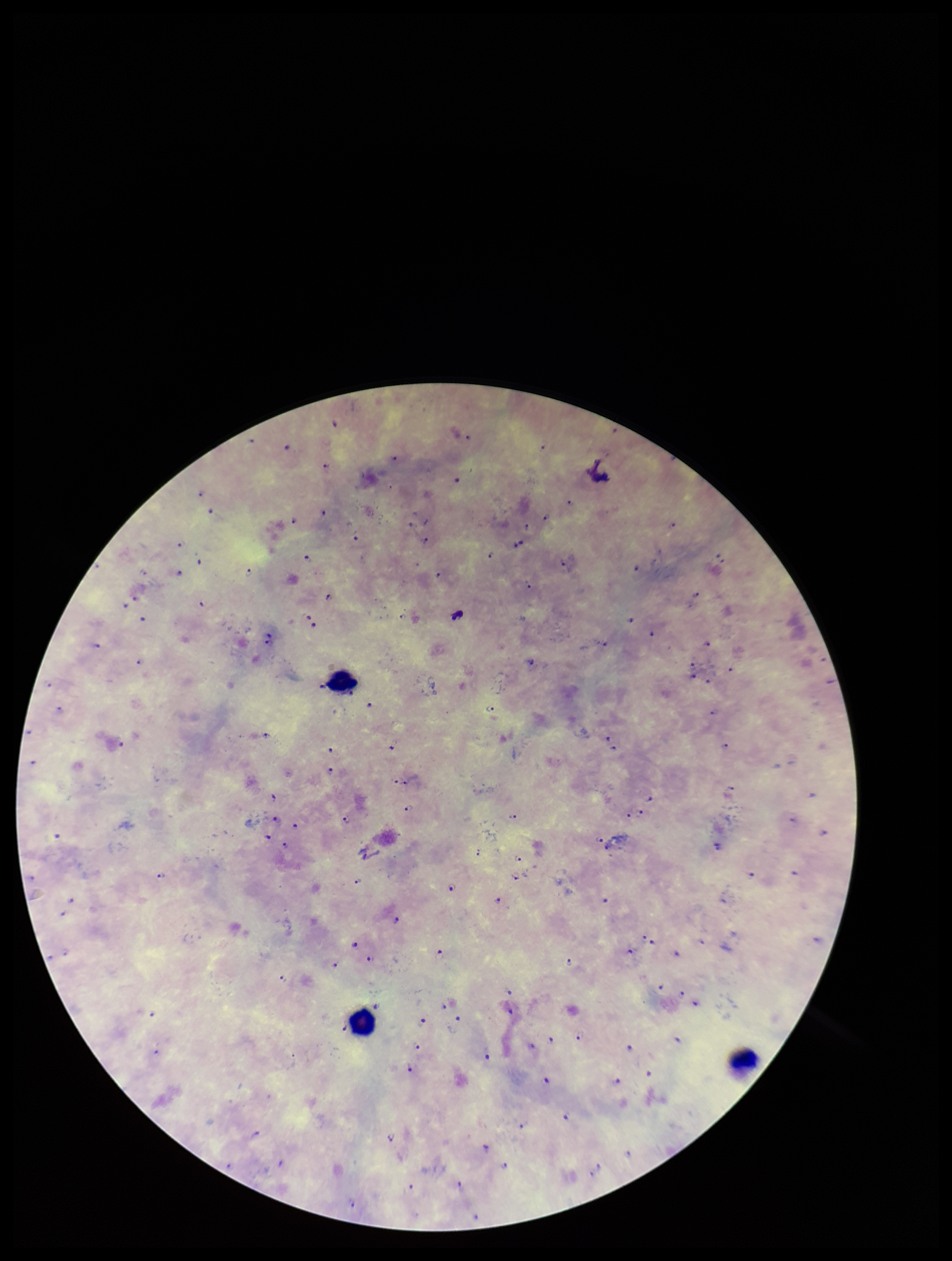
Summary:
  - Patient malaria status: positive
  - Leukocyte count: 3
  - Preparation: thick blood smear
  - Species reported for this patient: Plasmodium falciparum
  - Stain: Giemsa
  - Capture: smartphone photograph through the microscope eyepiece
  - Parasite count: 124
  - Image size: 952×1261 pixels
  - Field of view: single
  - Plasmodium parasites: identified